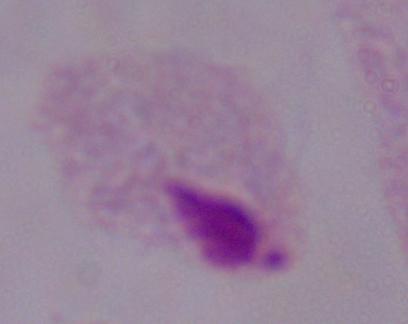
modality = photomicrograph
identification = trichomonad
magnification = 1000x